Report the malaria status of this cell.
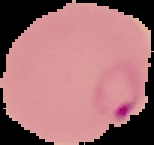
Parasitized.

Image is 154×145 pixels. From a thin blood smear. The area outside the segmented cell region is set to black.